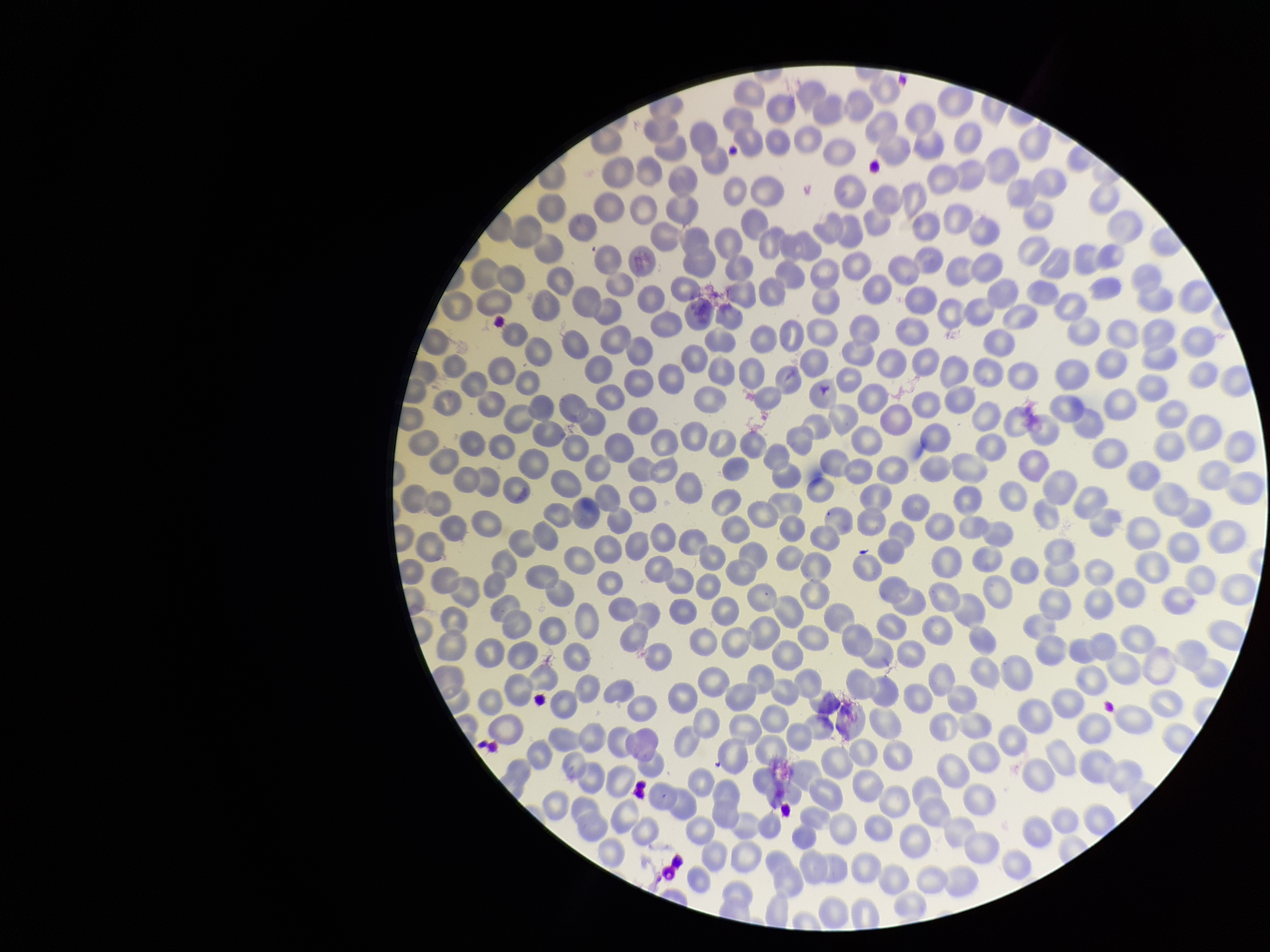

capture = smartphone photograph through the microscope eyepiece
stain = Giemsa
parasitized red blood cell count = 0
patient malaria status = infected
species reported for this patient = Plasmodium falciparum
red blood cell count = 324
parasitized red blood cells = none detected
field of view = single
image size = 1270×952 pixels
preparation = thin